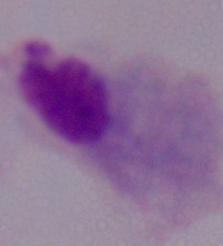
identification = trichomonad
modality = photomicrograph
magnification = 1000x